Assess this cell for malaria.
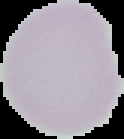
It is uninfected.

Summary:
  - Image type: segmented cell region with the area outside set to black
  - Image size: 124×139 pixels
  - Preparation: thin blood film